Comment on the morphology of the red blood cells.
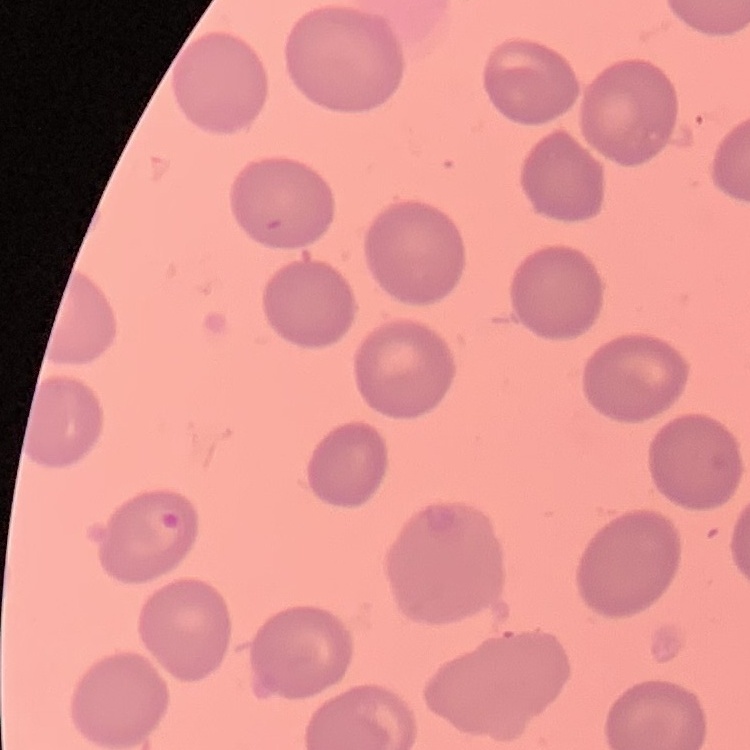
No rouleaux formation.

image type = square crop of a larger photomicrograph
preparation = thin blood film
stain = Field's or Giemsa